Report the malaria status of this cell.
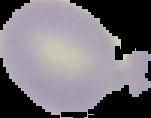

It is uninfected.

The area outside the segmented cell region is set to black. From a thin blood film. Image is 151×118 pixels.